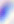

Summary:
  - Identification: Toxoplasma gondii
  - Magnification: 400x
  - Modality: micrograph